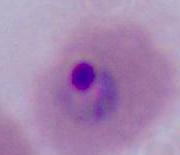

A Plasmodium parasite is seen. Captured at either 400x or 1000x magnification. Photomicrograph.